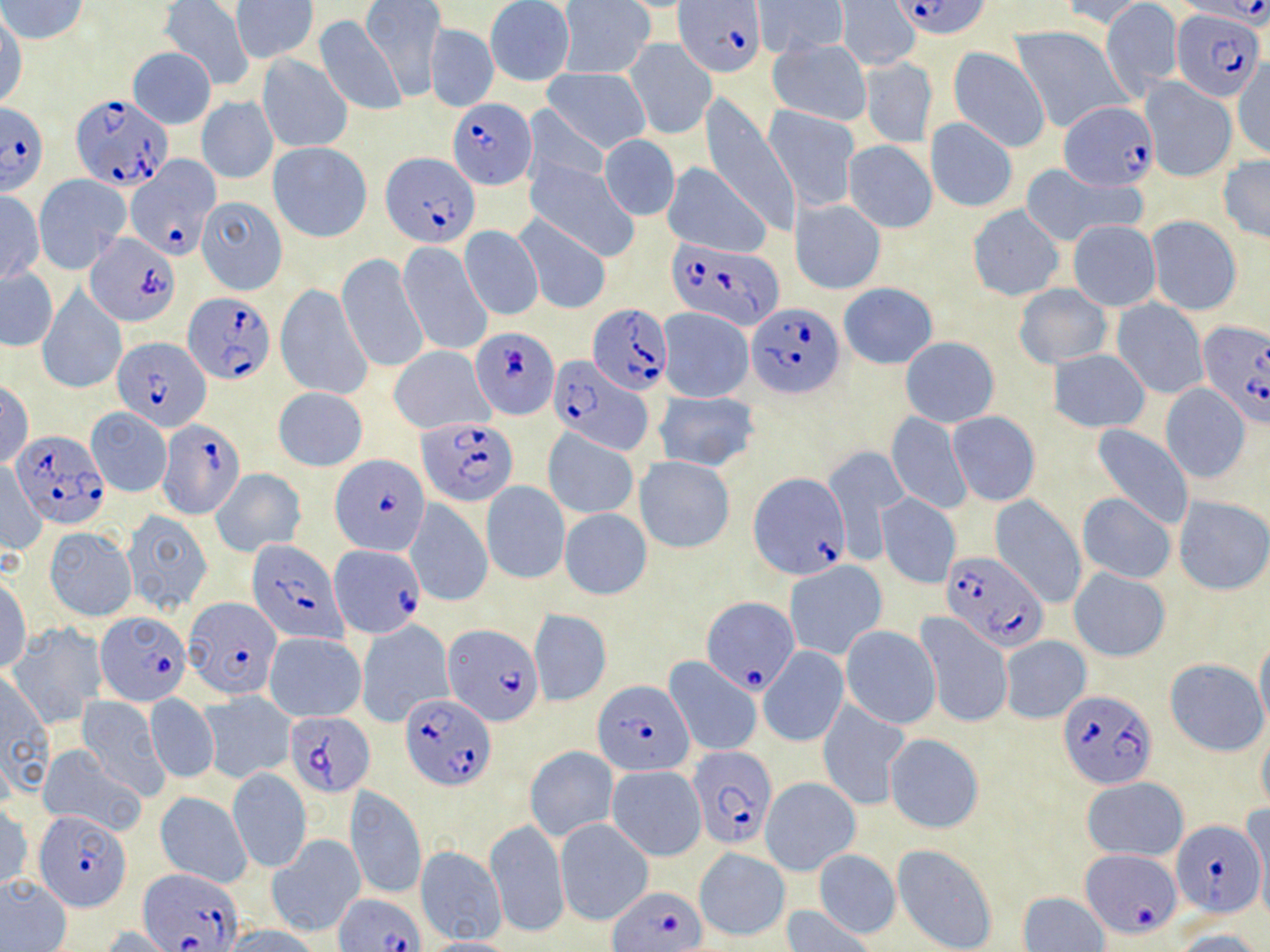
Approximate bounding boxes as named x1/y1/x2/y2 corners in pixels. Plasmodium falciparum-infected red blood cell locations (subset): (x1=677, y1=0, x2=767, y2=77), (x1=896, y1=0, x2=992, y2=41), (x1=1184, y1=0, x2=1270, y2=26), (x1=1172, y1=7, x2=1264, y2=102), (x1=71, y1=93, x2=173, y2=191), (x1=449, y1=98, x2=535, y2=189), (x1=1060, y1=100, x2=1157, y2=192), (x1=0, y1=101, x2=48, y2=195), (x1=382, y1=151, x2=479, y2=249), (x1=121, y1=154, x2=218, y2=266), (x1=86, y1=233, x2=181, y2=328), (x1=666, y1=237, x2=781, y2=327), (x1=182, y1=295, x2=273, y2=385), (x1=747, y1=302, x2=844, y2=398), (x1=588, y1=303, x2=673, y2=395), (x1=1198, y1=319, x2=1270, y2=425), (x1=471, y1=327, x2=558, y2=417), (x1=112, y1=335, x2=210, y2=433), (x1=549, y1=355, x2=647, y2=451), (x1=418, y1=416, x2=517, y2=506), (x1=157, y1=418, x2=245, y2=518), (x1=12, y1=431, x2=109, y2=527), (x1=331, y1=454, x2=430, y2=557), (x1=750, y1=472, x2=851, y2=579), (x1=329, y1=548, x2=424, y2=638), (x1=942, y1=551, x2=1046, y2=649), (x1=702, y1=595, x2=800, y2=693), (x1=186, y1=596, x2=281, y2=698), (x1=95, y1=611, x2=190, y2=705), (x1=444, y1=624, x2=543, y2=726), (x1=594, y1=682, x2=698, y2=777), (x1=400, y1=691, x2=495, y2=789), (x1=1058, y1=691, x2=1156, y2=787), (x1=285, y1=713, x2=374, y2=796), (x1=689, y1=746, x2=776, y2=850), (x1=36, y1=807, x2=129, y2=910), (x1=1171, y1=819, x2=1264, y2=918), (x1=1083, y1=849, x2=1181, y2=937), (x1=140, y1=869, x2=245, y2=951), (x1=610, y1=884, x2=704, y2=950), (x1=334, y1=892, x2=425, y2=952). Uninfected red blood cell locations (subset): (x1=1, y1=0, x2=89, y2=44), (x1=835, y1=0, x2=919, y2=71), (x1=1057, y1=0, x2=1152, y2=31), (x1=159, y1=1, x2=253, y2=90), (x1=231, y1=1, x2=319, y2=63), (x1=359, y1=1, x2=446, y2=99), (x1=484, y1=1, x2=574, y2=85), (x1=557, y1=1, x2=655, y2=77), (x1=754, y1=2, x2=847, y2=55), (x1=1101, y1=2, x2=1183, y2=98), (x1=0, y1=9, x2=26, y2=112), (x1=313, y1=14, x2=406, y2=116), (x1=425, y1=22, x2=498, y2=112), (x1=1012, y1=25, x2=1131, y2=133), (x1=626, y1=40, x2=716, y2=140), (x1=767, y1=40, x2=871, y2=125), (x1=949, y1=46, x2=1050, y2=152), (x1=127, y1=47, x2=216, y2=129), (x1=257, y1=53, x2=353, y2=153), (x1=861, y1=57, x2=937, y2=147), (x1=1232, y1=59, x2=1269, y2=160), (x1=541, y1=67, x2=649, y2=154), (x1=1140, y1=76, x2=1238, y2=181), (x1=197, y1=95, x2=277, y2=185), (x1=699, y1=96, x2=801, y2=237), (x1=520, y1=104, x2=611, y2=196), (x1=765, y1=104, x2=859, y2=212), (x1=925, y1=118, x2=1018, y2=211), (x1=600, y1=135, x2=679, y2=221), (x1=844, y1=140, x2=937, y2=233), (x1=268, y1=143, x2=372, y2=241), (x1=1217, y1=155, x2=1270, y2=243), (x1=527, y1=161, x2=639, y2=260), (x1=662, y1=161, x2=773, y2=259), (x1=1020, y1=164, x2=1144, y2=246), (x1=34, y1=174, x2=129, y2=272), (x1=1, y1=191, x2=44, y2=284), (x1=196, y1=196, x2=286, y2=295), (x1=791, y1=198, x2=886, y2=295), (x1=967, y1=205, x2=1066, y2=301), (x1=515, y1=213, x2=611, y2=315), (x1=1146, y1=215, x2=1242, y2=315), (x1=1067, y1=219, x2=1161, y2=310), (x1=458, y1=225, x2=544, y2=321), (x1=396, y1=241, x2=493, y2=357), (x1=337, y1=253, x2=428, y2=373), (x1=1, y1=269, x2=58, y2=351), (x1=837, y1=282, x2=938, y2=369), (x1=276, y1=283, x2=373, y2=401), (x1=1018, y1=283, x2=1111, y2=369), (x1=37, y1=287, x2=126, y2=393), (x1=1112, y1=299, x2=1209, y2=398), (x1=658, y1=306, x2=754, y2=403), (x1=900, y1=337, x2=999, y2=427), (x1=388, y1=345, x2=494, y2=433), (x1=1050, y1=349, x2=1151, y2=433), (x1=0, y1=381, x2=34, y2=467), (x1=1160, y1=383, x2=1253, y2=485), (x1=273, y1=387, x2=368, y2=472), (x1=653, y1=391, x2=760, y2=473), (x1=86, y1=407, x2=172, y2=498), (x1=887, y1=412, x2=970, y2=516), (x1=946, y1=413, x2=1041, y2=507), (x1=1088, y1=425, x2=1194, y2=532), (x1=544, y1=430, x2=639, y2=519), (x1=823, y1=445, x2=911, y2=556), (x1=635, y1=456, x2=735, y2=553), (x1=1, y1=465, x2=46, y2=556), (x1=211, y1=467, x2=307, y2=556), (x1=481, y1=480, x2=569, y2=584), (x1=1077, y1=493, x2=1176, y2=583), (x1=877, y1=494, x2=960, y2=588), (x1=990, y1=496, x2=1086, y2=606), (x1=1173, y1=496, x2=1270, y2=594), (x1=405, y1=498, x2=492, y2=608), (x1=559, y1=508, x2=652, y2=600), (x1=120, y1=510, x2=212, y2=614), (x1=43, y1=527, x2=137, y2=621), (x1=784, y1=560, x2=887, y2=659), (x1=1069, y1=567, x2=1170, y2=662), (x1=0, y1=578, x2=32, y2=673), (x1=529, y1=609, x2=611, y2=706), (x1=917, y1=614, x2=1011, y2=728), (x1=356, y1=620, x2=454, y2=727), (x1=8, y1=623, x2=106, y2=729), (x1=840, y1=625, x2=941, y2=729), (x1=264, y1=631, x2=366, y2=722), (x1=999, y1=636, x2=1091, y2=724), (x1=1254, y1=636, x2=1270, y2=736), (x1=760, y1=646, x2=848, y2=746), (x1=665, y1=656, x2=762, y2=756), (x1=1164, y1=657, x2=1267, y2=755), (x1=1, y1=671, x2=54, y2=802), (x1=199, y1=691, x2=296, y2=783), (x1=144, y1=693, x2=219, y2=783), (x1=76, y1=696, x2=170, y2=800), (x1=818, y1=699, x2=910, y2=811), (x1=1256, y1=725, x2=1270, y2=814), (x1=884, y1=733, x2=984, y2=834), (x1=36, y1=744, x2=147, y2=836), (x1=524, y1=747, x2=619, y2=841), (x1=606, y1=765, x2=706, y2=860), (x1=227, y1=767, x2=311, y2=873), (x1=761, y1=777, x2=860, y2=874), (x1=1083, y1=777, x2=1189, y2=862), (x1=345, y1=786, x2=427, y2=900), (x1=156, y1=792, x2=252, y2=888), (x1=0, y1=804, x2=33, y2=894), (x1=1250, y1=810, x2=1269, y2=923), (x1=485, y1=818, x2=571, y2=941), (x1=553, y1=818, x2=653, y2=926), (x1=266, y1=834, x2=365, y2=936), (x1=891, y1=843, x2=998, y2=952), (x1=415, y1=846, x2=506, y2=943), (x1=695, y1=848, x2=790, y2=941), (x1=813, y1=848, x2=902, y2=940), (x1=0, y1=874, x2=72, y2=951), (x1=1018, y1=891, x2=1109, y2=952), (x1=781, y1=903, x2=877, y2=952), (x1=97, y1=925, x2=186, y2=952), (x1=221, y1=925, x2=326, y2=952), (x1=1169, y1=928, x2=1267, y2=952), (x1=416, y1=937, x2=520, y2=952). Slide-level diagnosis: Plasmodium falciparum. Optical microscopy. May-Grünwald-Giemsa stain. Thin blood smear. Captured at 1000x magnification. Single field of view. Image is 1270×952 pixels.